Outline platelets.
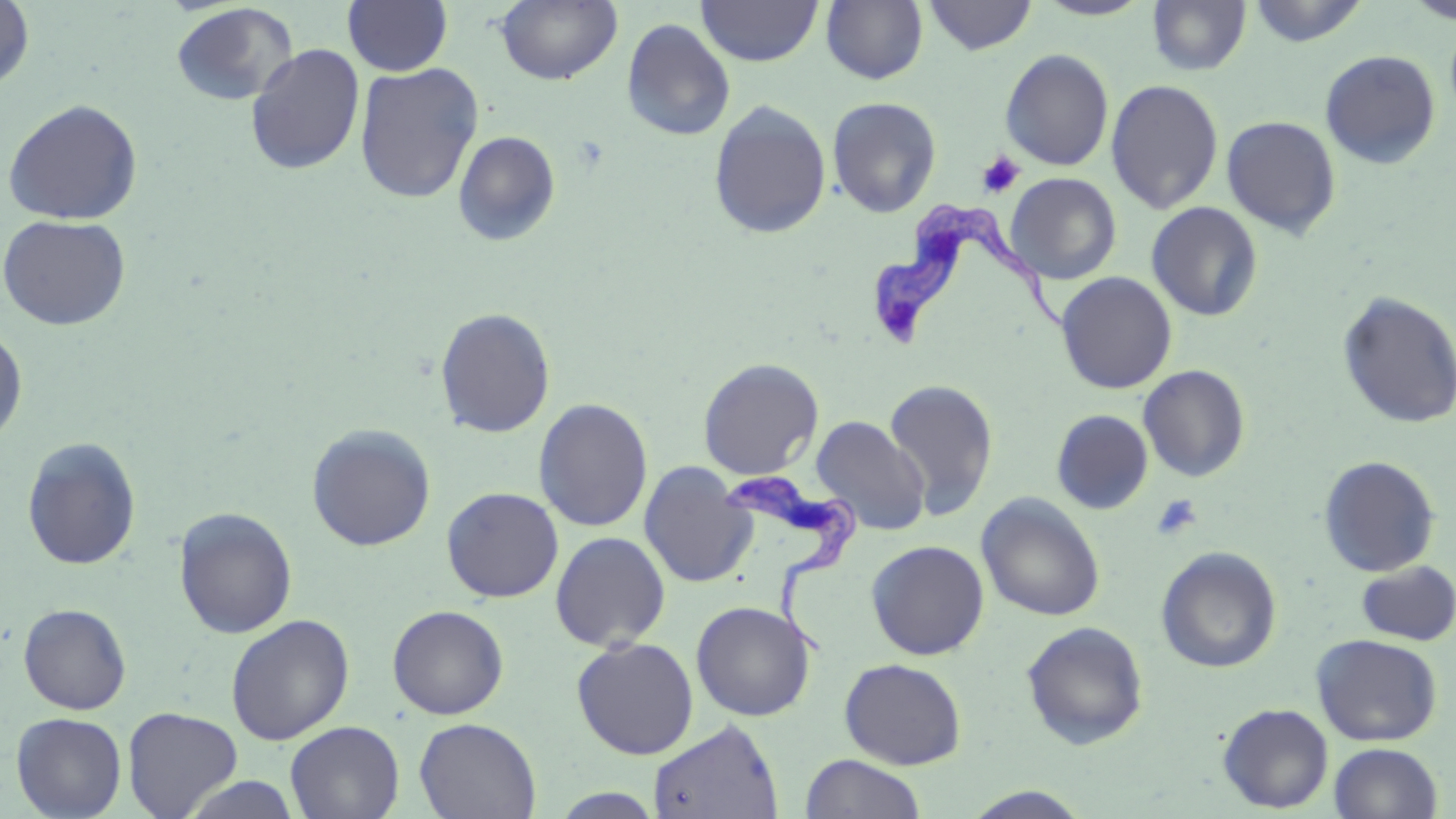

Approximate bounding boxes as (x1,y1)-(x2,y2) corner pairs in pixels.
Platelets: (976,151)-(1025,199), (1151,494)-(1203,541).

Uninfected red blood cell locations: (1,0)-(35,92), (821,0)-(928,85), (923,0)-(1038,55), (1033,0)-(1155,20), (1247,0)-(1369,46), (1404,0)-(1456,25), (343,1)-(453,76), (496,1)-(623,86), (697,1)-(823,66), (1147,1)-(1252,76), (170,2)-(299,107), (1444,16)-(1456,121), (621,18)-(735,141), (245,42)-(366,177), (1000,49)-(1114,171), (1320,50)-(1441,169), (354,62)-(484,203), (1106,79)-(1224,214), (826,96)-(942,218), (2,97)-(143,225), (708,99)-(832,239), (1221,115)-(1342,238), (452,130)-(561,247), (1006,172)-(1121,284), (1146,201)-(1263,322), (0,213)-(132,331), (1056,271)-(1178,394), (1336,290)-(1456,430), (434,307)-(555,438), (0,324)-(28,448), (698,358)-(823,480), (1138,365)-(1251,482), (883,380)-(999,520), (534,398)-(653,532), (1052,409)-(1153,514), (810,415)-(930,537), (306,423)-(436,551), (22,437)-(142,571), (1317,455)-(1440,577), (639,462)-(756,588), (441,486)-(563,602), (976,493)-(1106,622), (173,506)-(298,638), (550,531)-(671,652), (866,540)-(989,660), (1155,546)-(1282,673), (1355,560)-(1456,646), (690,600)-(816,721), (18,602)-(132,714), (387,605)-(509,720), (225,614)-(355,745), (1021,621)-(1149,750), (1311,633)-(1443,746), (571,636)-(699,759), (839,658)-(967,770), (1218,703)-(1334,813), (122,706)-(243,818), (11,712)-(127,819), (414,717)-(541,818), (647,718)-(784,819), (285,721)-(405,819), (1328,742)-(1443,819), (799,753)-(927,818), (178,774)-(304,818), (961,786)-(1095,818), (549,788)-(666,818). Trypanosoma brucei locations: (872,202)-(1079,352), (724,468)-(862,659). Slide-level diagnosis: Trypanosoma brucei. Captured at 1000x magnification. Image is 1456×819 pixels. Optical microscopy. One field of a larger specimen. Thin blood smear. May-Grünwald-Giemsa-stained preparation.